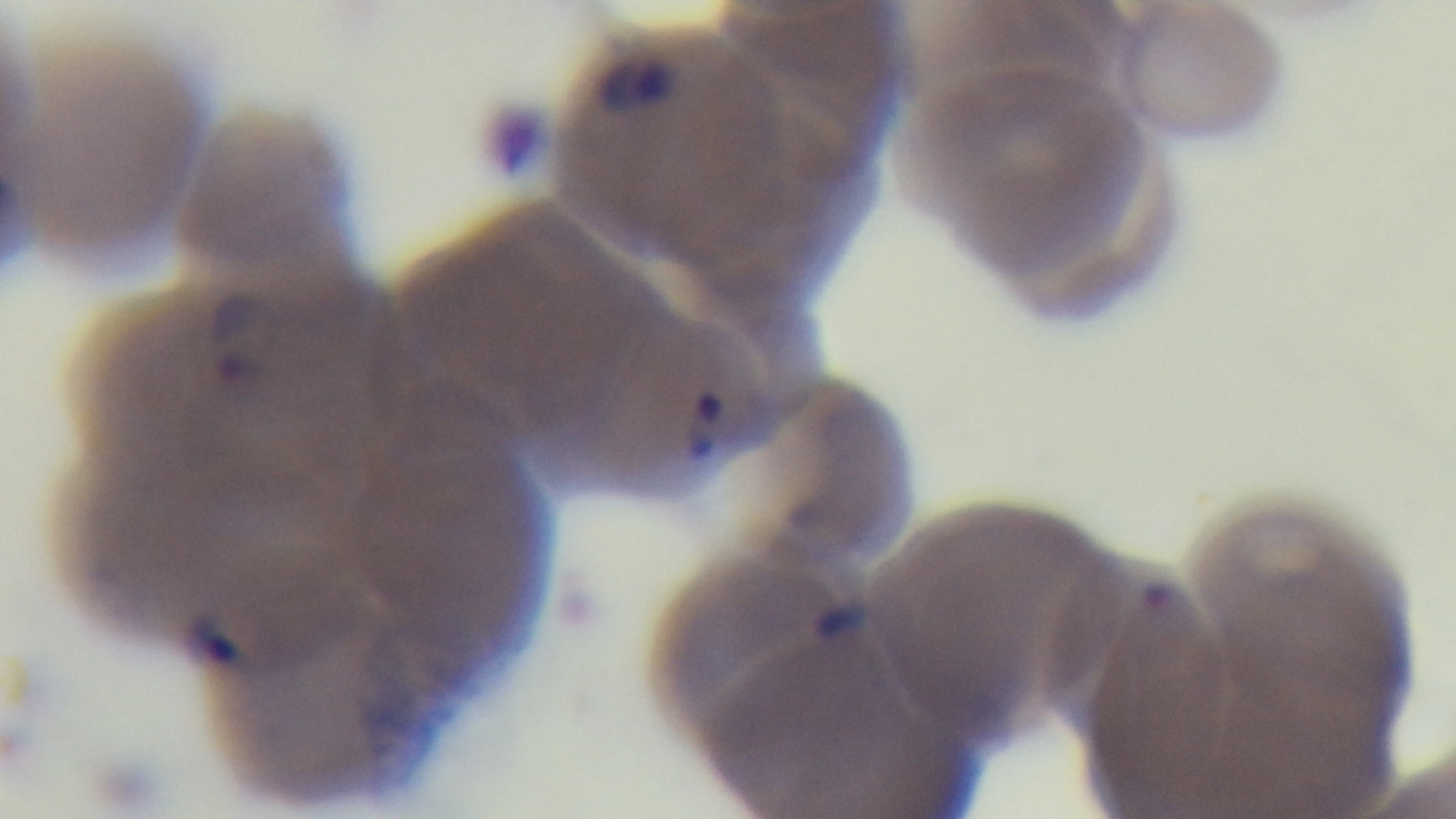

Giemsa-stained. 100x oil-immersion objective. Preparation: thin. Single field of view. Mounted 4K digital camera. Malaria status: infected. Light microscopy.